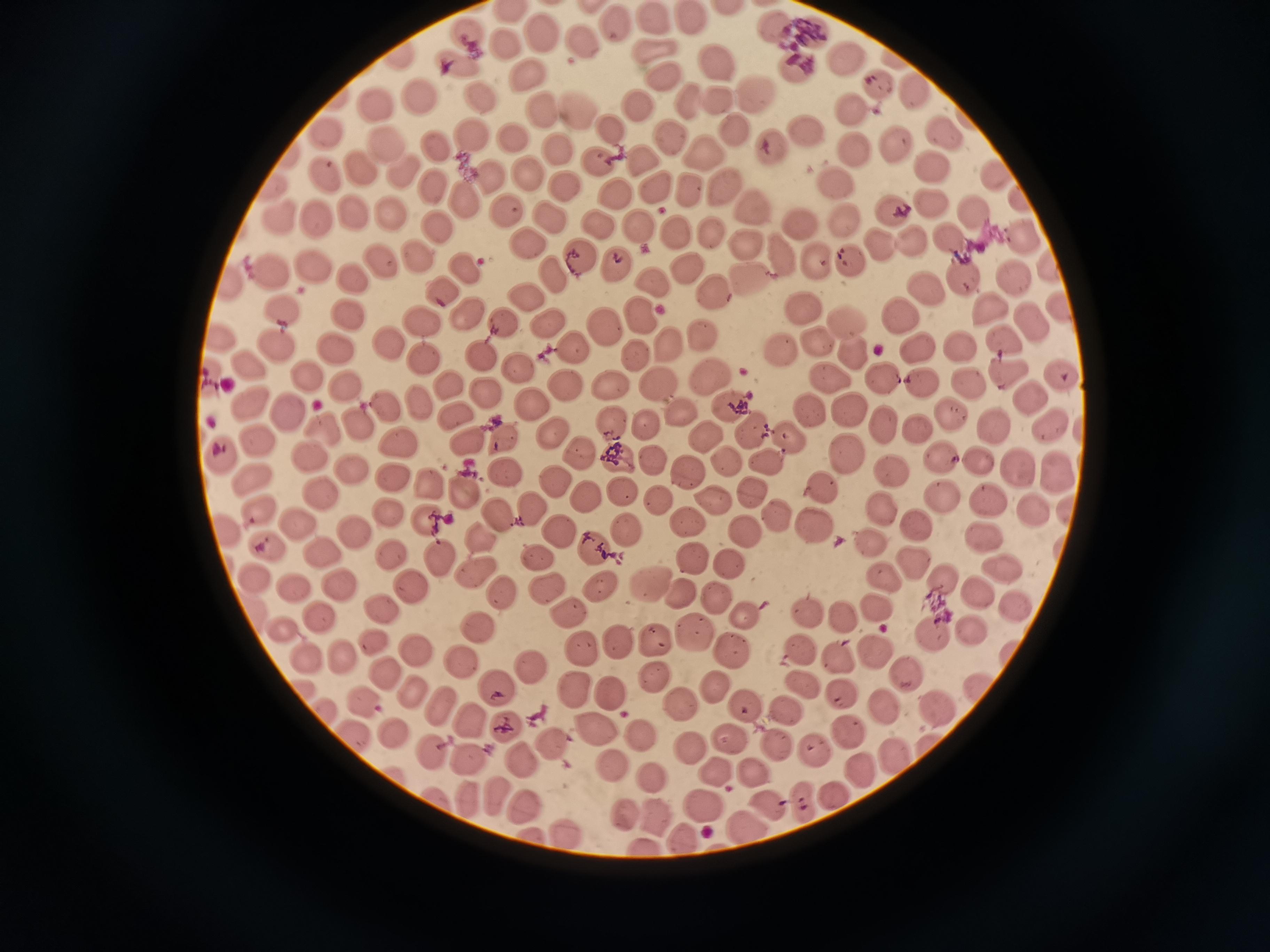
cell locations = approximate centers as (x, y) in pixels: (730, 9), (690, 18), (653, 20), (612, 21), (771, 25), (803, 31), (464, 35), (540, 36), (581, 36), (502, 46), (654, 50), (396, 57), (844, 58), (715, 59), (894, 59), (452, 63), (789, 65), (661, 71), (523, 78), (877, 82), (914, 91), (421, 95), (478, 95), (753, 95), (685, 99), (718, 100), (375, 102), (639, 106), (541, 110), (582, 110), (853, 112), (615, 130), (736, 130), (941, 131), (807, 132), (323, 133), (669, 135), (473, 137), (514, 138), (435, 143), (769, 144), (895, 144), (383, 146), (558, 149), (849, 150), (704, 152), (287, 155), (643, 159), (600, 163), (932, 165), (362, 168), (402, 169), (992, 171), (323, 172), (491, 173), (526, 175), (834, 182), (434, 184), (570, 185), (656, 187), (270, 189), (724, 189), (693, 191), (616, 195), (1018, 199), (466, 200), (931, 203), (749, 208), (510, 209), (973, 211), (892, 212), (352, 214), (391, 215), (283, 218), (840, 218), (317, 219), (552, 219), (595, 223), (799, 224), (637, 225), (439, 231), (676, 232), (709, 234), (1020, 237), (950, 239), (910, 240), (747, 244), (527, 245), (876, 245), (576, 255), (778, 255), (417, 256), (815, 258), (382, 261), (848, 262), (313, 264), (466, 265), (1048, 265), (619, 266), (689, 269), (269, 270), (355, 276), (552, 276), (961, 277), (1016, 278), (652, 281), (751, 281), (229, 285), (441, 288), (925, 288), (714, 292), (527, 297), (803, 304), (991, 307), (1053, 308), (284, 310), (469, 312), (345, 313), (638, 314), (899, 314), (501, 321), (843, 321), (1029, 321), (421, 322), (605, 324), (545, 325), (699, 332), (217, 337), (1002, 339), (386, 342), (818, 344), (672, 345), (961, 345), (576, 346), (918, 347), (276, 348), (341, 351), (777, 352), (479, 353), (853, 354), (416, 355), (639, 356), (247, 362), (520, 369), (1061, 374), (1006, 375), (206, 377), (711, 378), (828, 378), (304, 379), (883, 379), (921, 383), (562, 384), (970, 384), (344, 385), (614, 387), (444, 388), (656, 388), (486, 395), (1030, 398), (527, 400), (247, 402), (416, 402), (385, 406), (731, 406), (807, 408), (683, 409), (285, 411), (850, 411), (949, 412), (456, 414), (612, 424), (644, 424), (359, 425), (883, 425), (1051, 425), (996, 426), (327, 428), (919, 428), (752, 430), (551, 434), (787, 434), (258, 438), (464, 439), (706, 439), (503, 442), (398, 443), (307, 452), (579, 452), (848, 452), (222, 453), (940, 457), (978, 457), (649, 458), (620, 459), (768, 460), (725, 461), (349, 469), (1020, 470), (893, 471), (506, 473), (687, 473), (1058, 474), (251, 476), (392, 476), (427, 483), (557, 484), (822, 488), (461, 491), (751, 491), (319, 493), (623, 495), (941, 496), (657, 499), (713, 500), (990, 500), (589, 502), (528, 508), (881, 508), (1069, 508), (1028, 509), (257, 511), (778, 514), (387, 515), (497, 518), (689, 520), (299, 522), (425, 522), (915, 524), (815, 527), (221, 529), (625, 530), (747, 532), (353, 533), (557, 533), (476, 535), (984, 536), (872, 545), (265, 547), (594, 548), (321, 551), (391, 555), (533, 556), (691, 557), (436, 560), (913, 560), (733, 563), (1008, 570), (475, 572), (883, 576), (256, 577), (945, 581), (650, 582), (336, 583), (601, 584), (410, 585), (548, 585), (293, 589), (502, 593), (683, 593), (977, 593), (715, 595), (880, 606), (1017, 607), (571, 610), (250, 611), (378, 611), (808, 612), (742, 614), (841, 617), (319, 618), (477, 628), (970, 630), (280, 631), (696, 631), (933, 635), (657, 639), (618, 641), (375, 642), (730, 646), (413, 649), (799, 649), (1006, 651), (584, 652), (875, 653), (344, 659), (839, 659), (305, 662), (463, 663), (531, 667), (384, 671), (653, 676), (905, 676), (805, 684), (497, 687), (570, 688), (713, 688), (412, 691), (979, 691), (611, 693), (842, 696), (360, 701), (682, 702), (744, 706), (884, 706), (444, 707), (938, 710), (325, 712), (785, 714), (470, 721), (509, 726), (844, 732), (393, 733), (597, 733), (641, 735), (353, 737), (727, 737), (553, 744), (689, 748), (776, 748), (892, 750), (430, 753), (814, 754), (468, 759), (522, 762), (611, 765), (716, 770), (754, 771), (862, 771), (393, 772), (652, 774), (438, 794), (827, 794), (496, 795), (469, 798), (798, 799), (765, 804), (699, 805), (525, 808), (625, 812), (656, 819), (746, 829), (567, 833), (534, 834), (684, 838), (642, 845)
field of view = single
capture = smartphone through the microscope eyepiece
preparation = thin blood smear
image size = 1270×952 pixels
stain = Giemsa